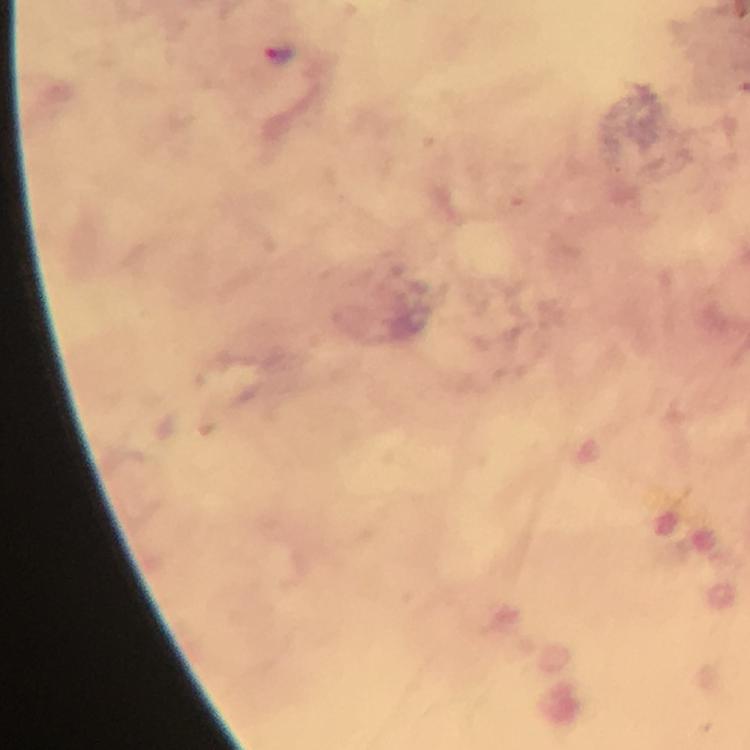
capture = smartphone photograph through a microscope
context = from a malaria diagnostic workup
image size = 750×750 pixels
cropped from = a single field of view
magnification = 100x
stain = Giemsa
malaria parasite locations = approximate centers as [x, y] in pixels: [280, 55]
immersion oil = applied
preparation = thick blood film